Name the parasite shown.
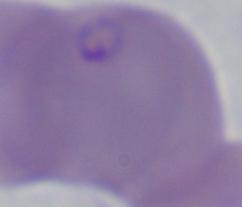
This is Babesia.

Summary:
  - Magnification: 1000x
  - Modality: photomicrograph